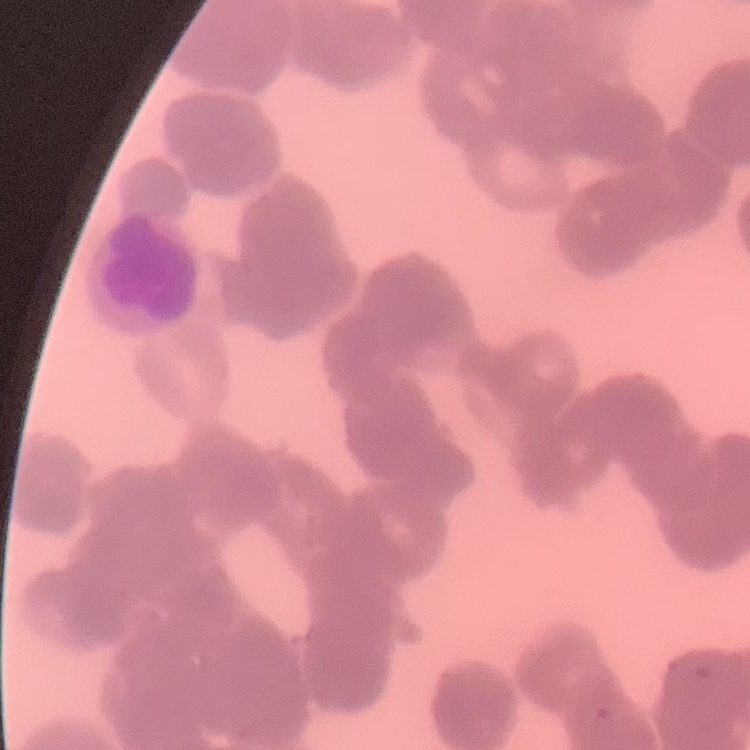

erythrocyte morphology = rouleaux formation
preparation = thin peripheral smear
image type = one tile cut from a larger photomicrograph
stain = Field's or Giemsa